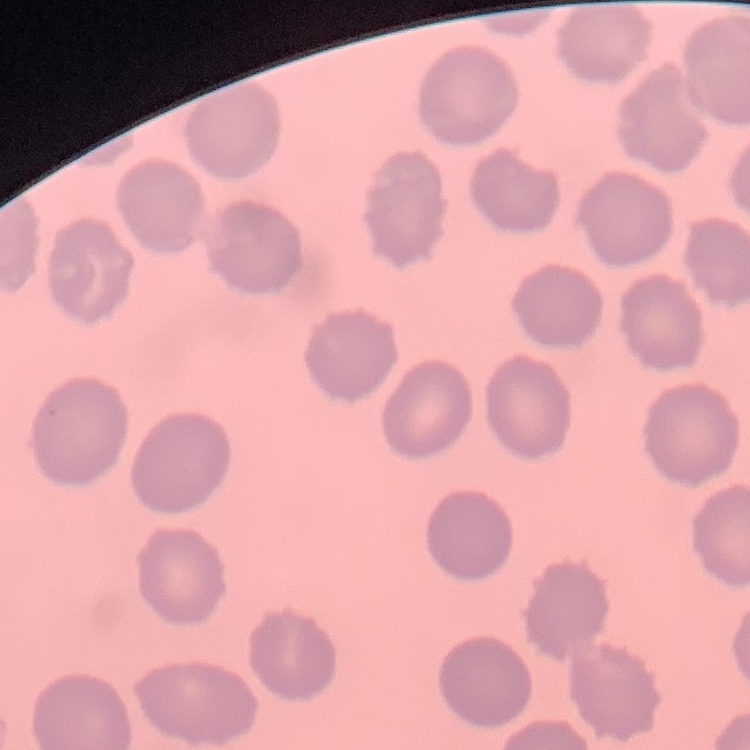

erythrocyte morphology = no rouleaux formation
stain = Field's or Giemsa
image type = square crop of a larger photomicrograph
preparation = thin blood smear